Locate every uninfected red blood cell.
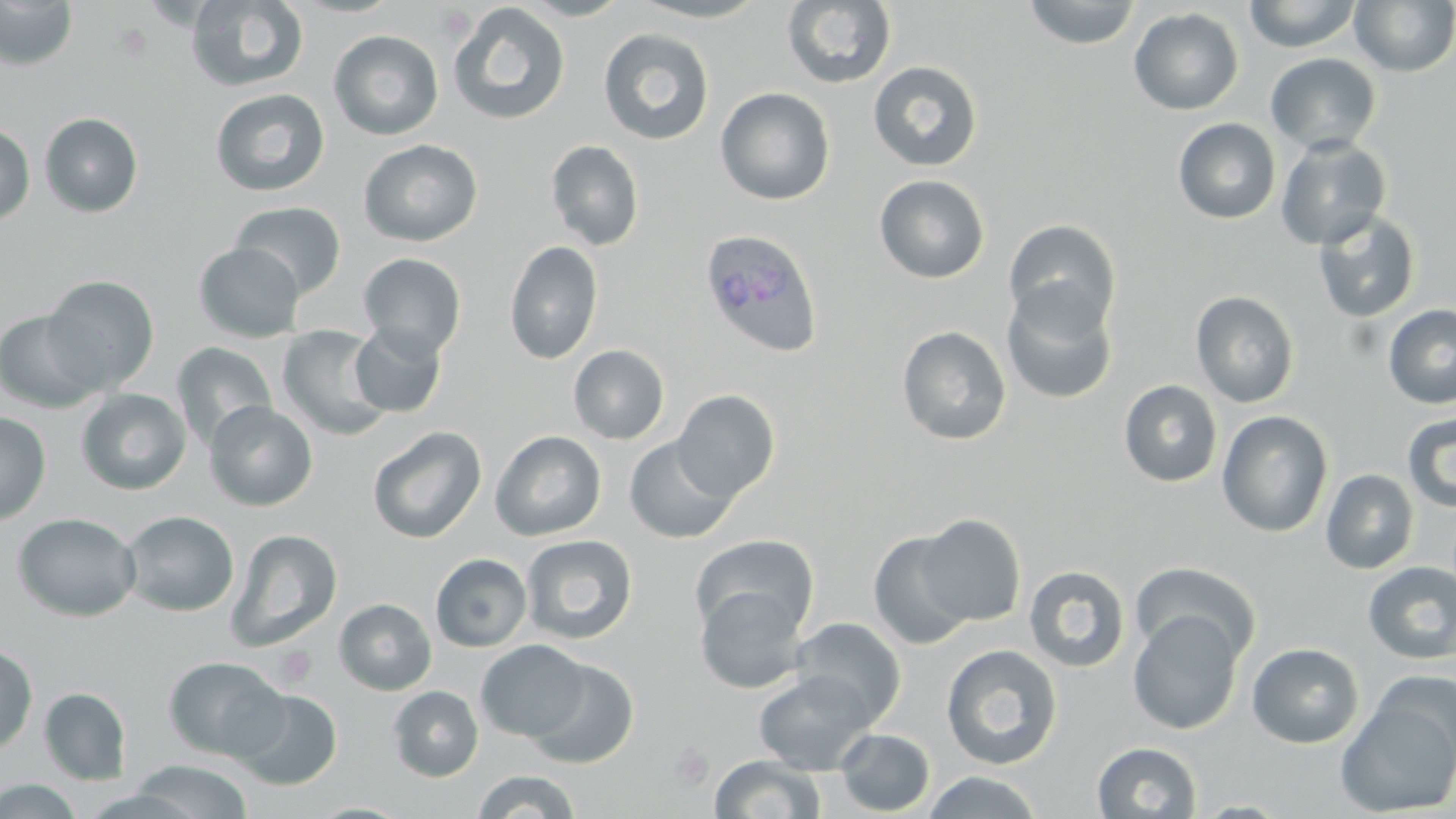

Approximate bounding boxes as (x1,y1)-(x2,y2) corner pairs in pixels.
Uninfected red blood cells: (184,0)-(309,93), (515,0)-(633,21), (625,0)-(771,22), (1022,0)-(1142,49), (1243,0)-(1362,53), (1350,0)-(1456,76), (0,1)-(78,70), (782,2)-(896,88), (447,3)-(571,126), (1128,7)-(1245,115), (598,28)-(714,146), (328,29)-(444,141), (1265,52)-(1382,155), (868,60)-(983,172), (715,87)-(835,206), (210,88)-(330,197), (39,112)-(144,217), (1173,118)-(1281,224), (0,122)-(35,225), (1275,135)-(1393,251), (358,139)-(483,247), (546,140)-(645,251), (874,174)-(991,283), (230,201)-(347,299), (1312,210)-(1422,324), (1003,219)-(1121,337), (504,240)-(603,365), (193,242)-(305,343), (358,252)-(467,358), (42,275)-(160,393), (1001,285)-(1118,404), (1191,290)-(1300,408), (1383,303)-(1456,409), (0,309)-(106,413), (349,322)-(447,418), (276,324)-(393,441), (897,325)-(1012,446), (171,342)-(278,450), (569,344)-(670,444), (1118,380)-(1223,487), (75,388)-(191,495), (673,388)-(781,500), (204,400)-(318,511), (1216,410)-(1334,537), (1401,411)-(1456,514), (0,412)-(51,526), (367,426)-(487,544), (490,430)-(607,541), (624,436)-(740,544), (1321,469)-(1419,574), (119,510)-(239,617), (13,512)-(141,622), (915,514)-(1027,626), (226,529)-(343,651), (867,530)-(977,651), (521,534)-(638,644), (690,534)-(819,640), (430,553)-(532,652), (1129,560)-(1260,665), (1363,561)-(1456,664), (1024,565)-(1130,673), (695,585)-(808,694), (334,598)-(437,695), (1127,609)-(1244,735), (791,616)-(907,725), (475,640)-(590,742), (1247,642)-(1364,748), (0,643)-(38,754), (941,644)-(1063,770), (163,656)-(287,761), (526,658)-(640,769), (753,670)-(875,774), (1335,684)-(1456,819), (388,686)-(483,782), (39,687)-(131,784), (233,689)-(343,791), (834,728)-(935,815), (1092,742)-(1202,819), (709,755)-(826,818), (129,759)-(253,818), (473,770)-(581,818), (920,770)-(1045,818), (0,778)-(83,818), (307,802)-(415,819).

Plasmodium ovale-infected red blood cell locations = approximate bounding boxes as (x1,y1)-(x2,y2) corner pairs in pixels: (698,227)-(823,358)
slide-level diagnosis = Plasmodium ovale
preparation = thin blood film
magnification = 1000x
platelet locations = approximate bounding boxes as (x1,y1)-(x2,y2) corner pairs in pixels: (433,4)-(476,40), (273,644)-(317,689), (667,741)-(714,791)
stain = May-Grünwald-Giemsa
modality = light microscopy
image size = 1456×819 pixels
field of view = one of a larger specimen